Outline each blood parasite and name the species.
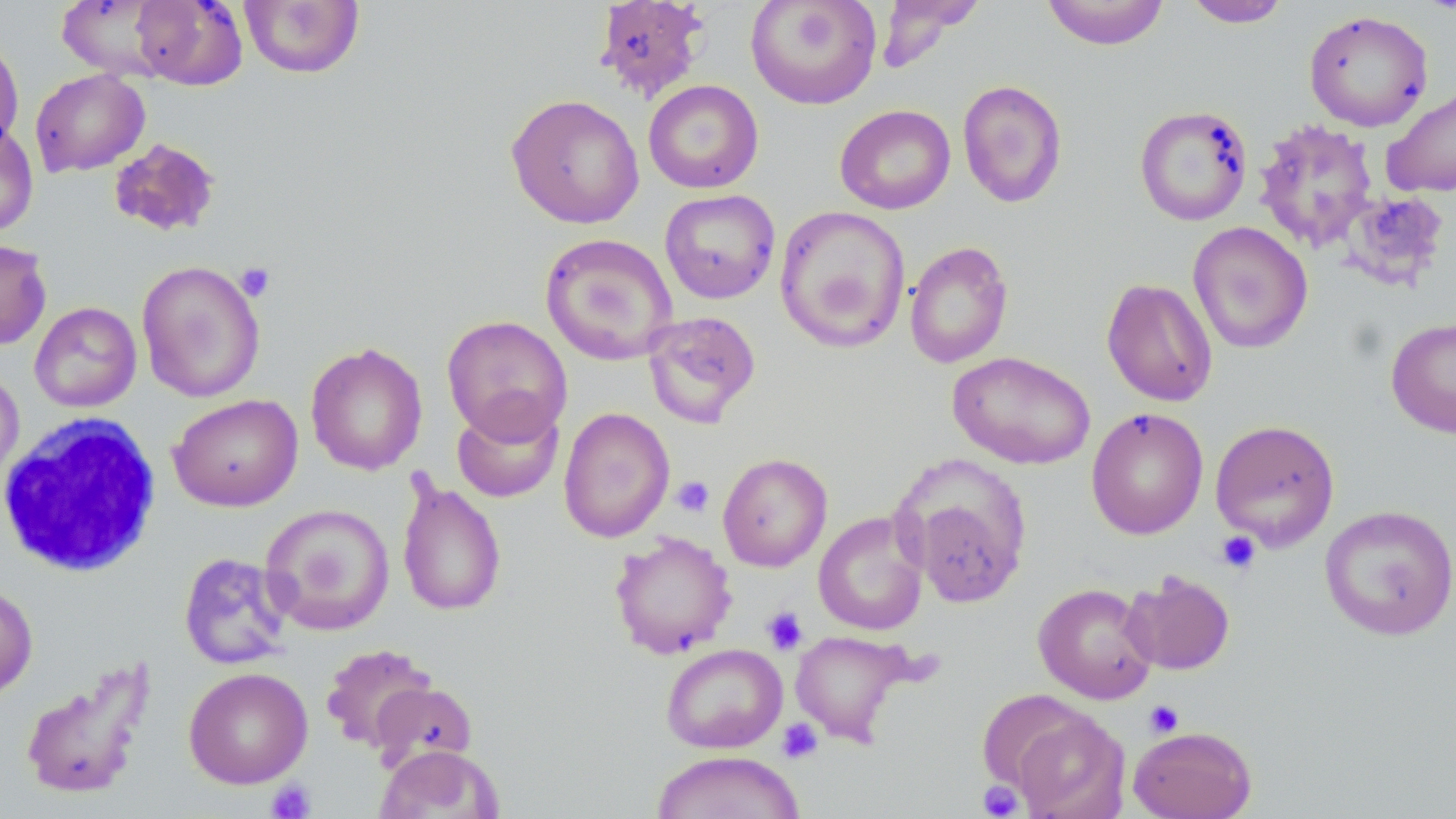

No blood parasites seen.

slide-level diagnosis = no evidence of blood parasites
modality = optical microscopy
white blood cell locations = approximate bounding boxes as (x1,y1)-(x2,y2) corner pairs in pixels: (0,412)-(163,578)
field of view = single
platelet locations = approximate bounding boxes as (x1,y1)-(x2,y2) corner pairs in pixels: (236,263)-(275,301), (672,476)-(715,517), (1216,531)-(1261,575), (762,606)-(808,654), (1144,700)-(1184,738), (777,718)-(824,764), (266,780)-(316,819), (978,781)-(1024,818)
image size = 1456×819 pixels
magnification = 1000x
stain = May-Grünwald-Giemsa
preparation = thin blood film
uninfected red blood cell locations = approximate bounding boxes as (x1,y1)-(x2,y2) corner pairs in pixels: (131,0)-(247,89), (594,0)-(709,103), (746,0)-(881,110), (876,0)-(984,71), (1040,0)-(1170,50), (1182,0)-(1293,28), (54,1)-(175,79), (239,1)-(365,79), (1303,9)-(1434,132), (0,34)-(24,155), (30,68)-(150,177), (643,79)-(764,194), (957,79)-(1067,208), (1381,86)-(1456,198), (506,94)-(645,229), (835,104)-(956,215), (1134,104)-(1253,226), (1253,119)-(1379,252), (0,122)-(39,238), (109,137)-(221,237), (659,189)-(781,304), (1339,190)-(1451,291), (774,205)-(911,353), (1187,221)-(1313,354), (540,232)-(679,366), (0,239)-(52,350), (904,241)-(1014,369), (136,260)-(266,403), (1101,278)-(1218,406), (29,302)-(142,413), (642,311)-(761,428), (441,315)-(573,443), (1386,317)-(1456,438), (305,341)-(428,476), (947,351)-(1096,470), (0,367)-(25,489), (168,394)-(303,512), (452,397)-(564,503), (558,406)-(675,543), (1086,407)-(1209,539), (1210,420)-(1340,551), (717,452)-(832,571), (896,456)-(1033,609), (397,474)-(507,619), (261,503)-(395,636), (1319,504)-(1456,640), (813,511)-(929,636), (609,532)-(737,659), (178,552)-(294,670), (1122,570)-(1235,675), (0,582)-(38,702), (1033,583)-(1158,704), (789,629)-(915,746), (320,643)-(437,753), (660,643)-(788,753), (18,660)-(155,802), (183,667)-(313,789), (369,681)-(477,773), (1008,707)-(1130,819), (1127,725)-(1257,819), (375,744)-(503,819), (650,750)-(805,819)